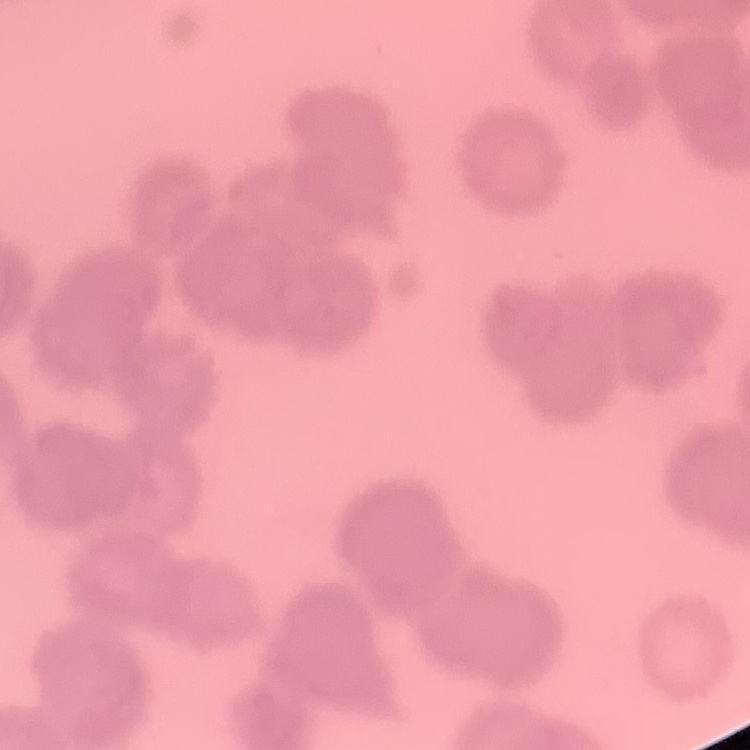
Summary:
  - Red blood cell morphology: rouleaux formation
  - Stain: Field's or Giemsa
  - Image type: one tile cut from a larger photomicrograph
  - Preparation: thin blood film